Identify the parasite.
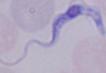

A trypanosome.

Photomicrograph. Captured at 1000x magnification.